Locate every leukocyte (white blood cell).
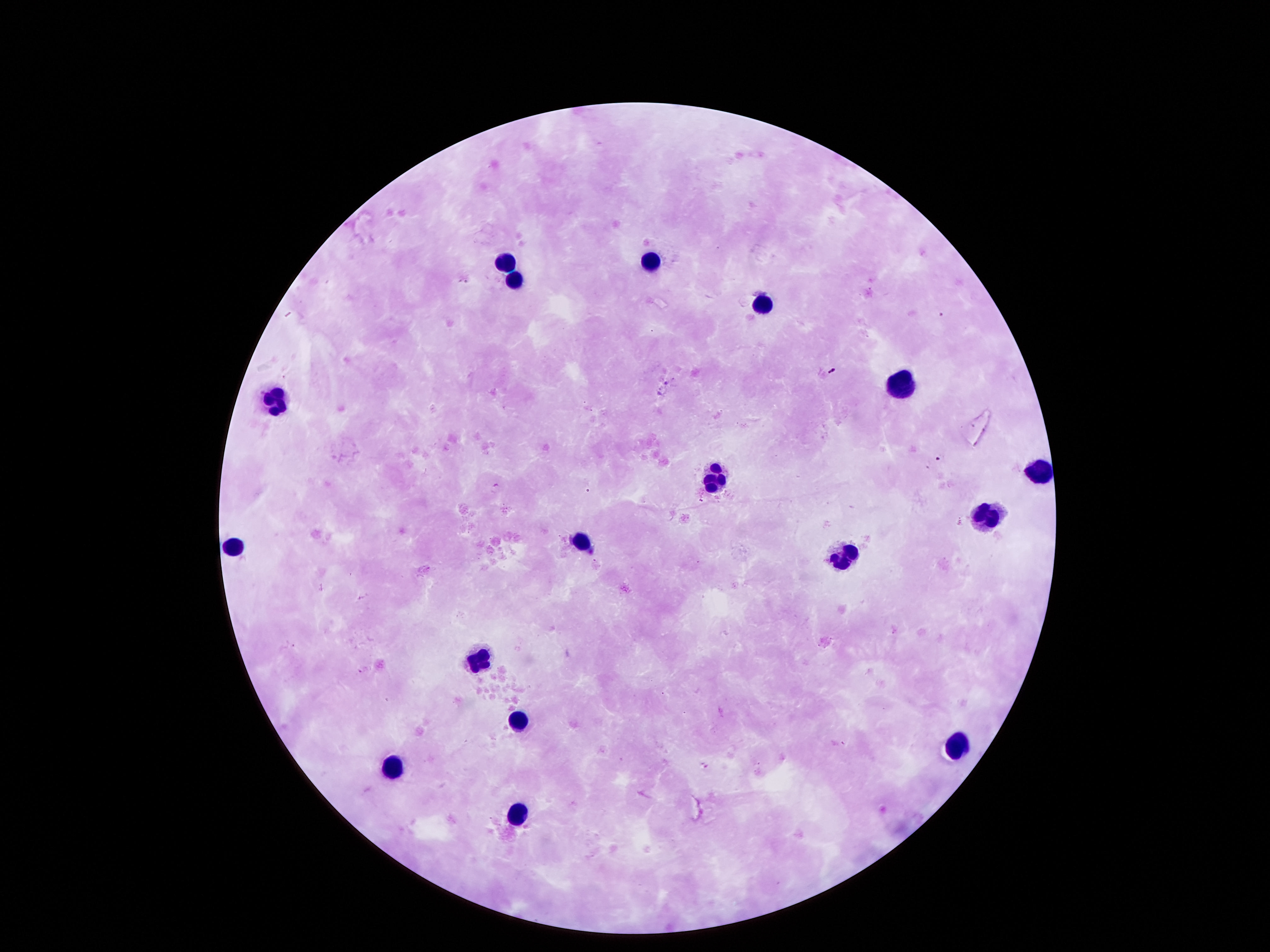
Approximate centers as [x, y] in pixels.
Leukocytes: [505, 261], [650, 263], [513, 280], [761, 303], [898, 383], [276, 402], [1040, 469], [711, 481], [982, 515], [578, 535], [230, 543], [841, 554], [478, 664], [517, 715], [956, 741], [387, 767], [513, 814].

Summary:
  - Patient malaria status: negative
  - Magnification: 100x
  - Field of view: single
  - Capture: smartphone camera through the microscope eyepiece
  - Image size: 1270×952 pixels
  - Preparation: thick blood film
  - Stain: Giemsa